Locate every blood parasite and identify its species.
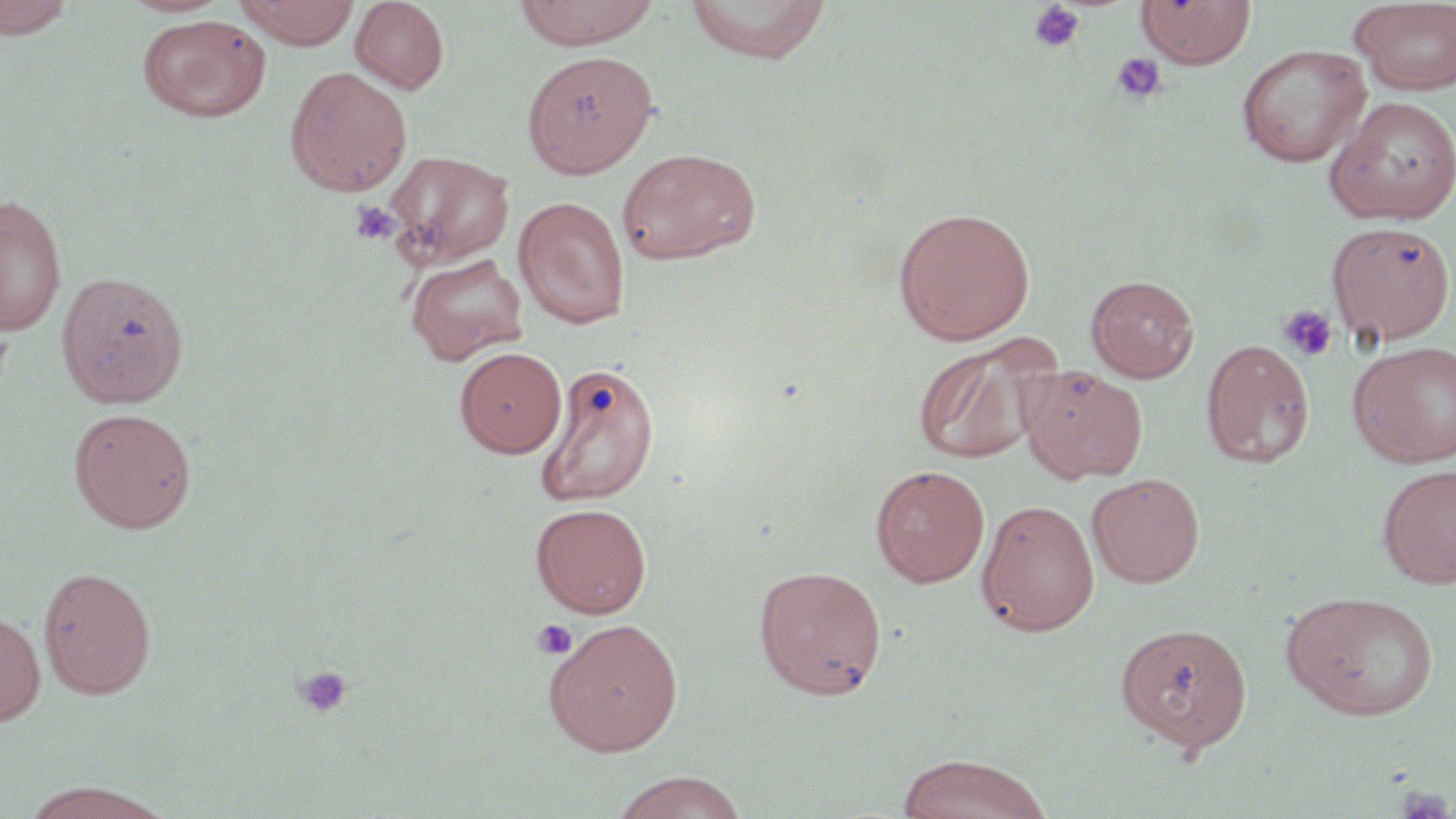
No blood parasites observed.

{
  "slide_level_diagnosis": "negative for blood parasites",
  "uninfected_red_blood_cell_locations": "approximate bounding boxes as [x1, y1, x2, y2] in pixels: [0, 0, 76, 40], [118, 0, 233, 17], [235, 0, 361, 48], [349, 0, 449, 93], [512, 0, 661, 49], [685, 0, 831, 63], [1136, 0, 1256, 68], [1350, 1, 1456, 97], [137, 13, 271, 122], [1237, 44, 1371, 167], [522, 50, 659, 177], [285, 66, 413, 197], [1324, 95, 1456, 225], [616, 147, 761, 265], [382, 150, 514, 269], [0, 193, 67, 336], [513, 196, 630, 329], [893, 206, 1036, 345], [1327, 221, 1455, 346], [406, 253, 529, 365], [56, 270, 190, 409], [1086, 275, 1199, 382], [911, 334, 1058, 466], [1201, 338, 1316, 468], [1348, 340, 1456, 468], [454, 347, 567, 458], [537, 361, 660, 507], [1019, 365, 1148, 483], [69, 407, 197, 533], [1377, 463, 1456, 587], [870, 464, 990, 587], [1087, 473, 1204, 587], [977, 499, 1099, 636], [530, 502, 652, 617], [753, 565, 887, 699], [38, 566, 156, 698], [1282, 589, 1439, 722], [0, 610, 46, 727], [543, 619, 684, 756], [1115, 621, 1253, 753], [897, 753, 1053, 819], [609, 771, 749, 819], [19, 781, 175, 819]",
  "platelet_locations": "approximate bounding boxes as [x1, y1, x2, y2] in pixels: [1028, 1, 1085, 54], [1109, 52, 1166, 106], [349, 201, 400, 245], [1278, 304, 1339, 363], [531, 619, 578, 660], [293, 665, 353, 720], [1391, 786, 1454, 819]",
  "field_of_view": "single",
  "modality": "optical microscopy",
  "preparation": "thin blood film",
  "magnification": "1000x",
  "stain": "May-Grünwald-Giemsa",
  "image_size": "1456×819 pixels"
}